Classify this cell by malaria status.
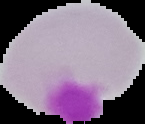
Uninfected.

preparation: thin blood film
image_type: segmented cell region with the area outside set to black
image_size: 145×124 pixels